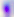 Captured at 400x magnification. Photomicrograph. Toxoplasma gondii is seen.